Identify the preparation type.
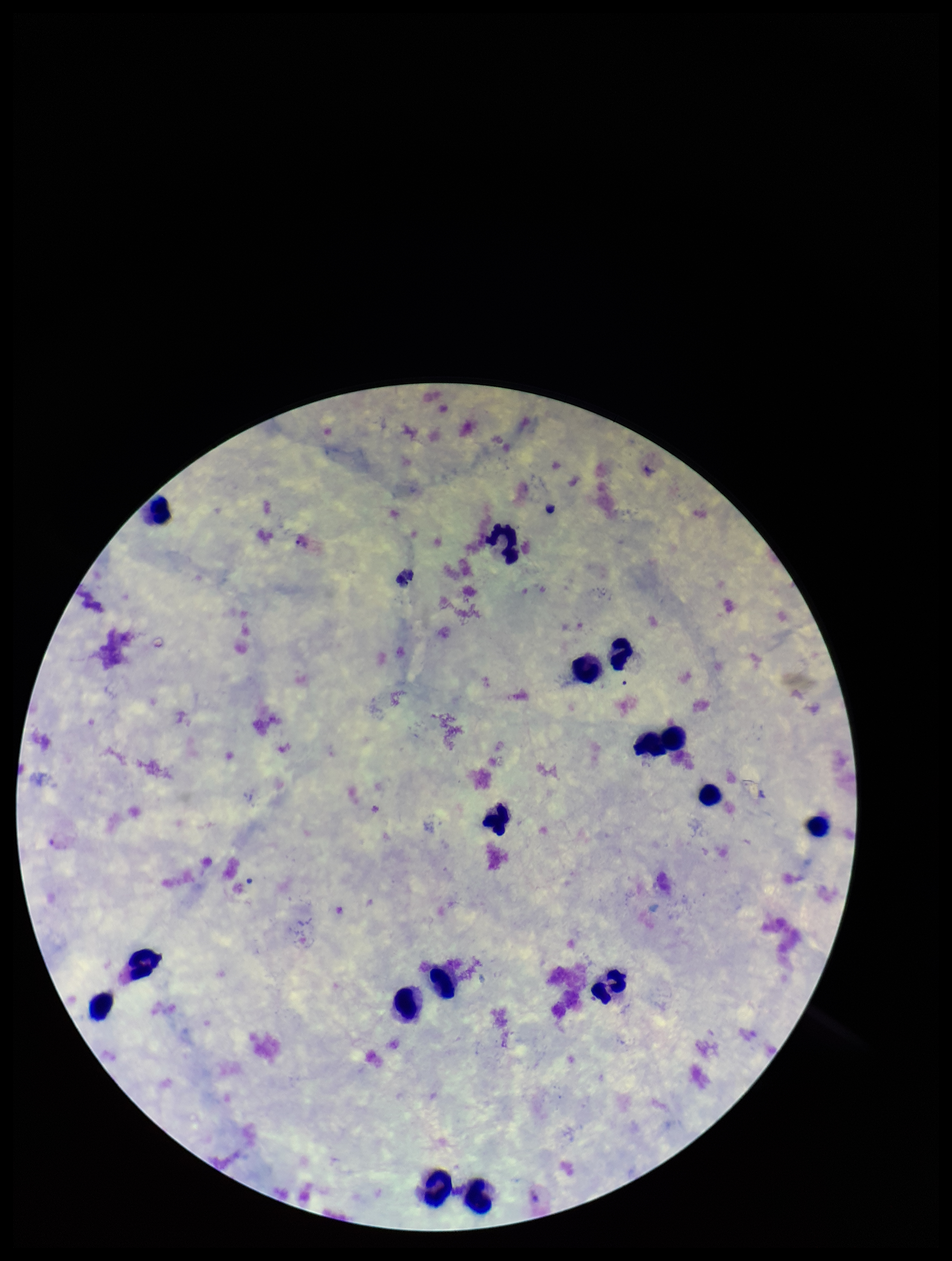

It is a thick blood smear.

Plasmodium parasites: detected. Single field of view. Species reported for this patient: Plasmodium vivax. Parasite count: 1. Stained with Giemsa. Patient malaria status: positive. Smartphone photograph taken through the eyepiece of a microscope. Leukocyte count: 16. Image is 952×1261 pixels.